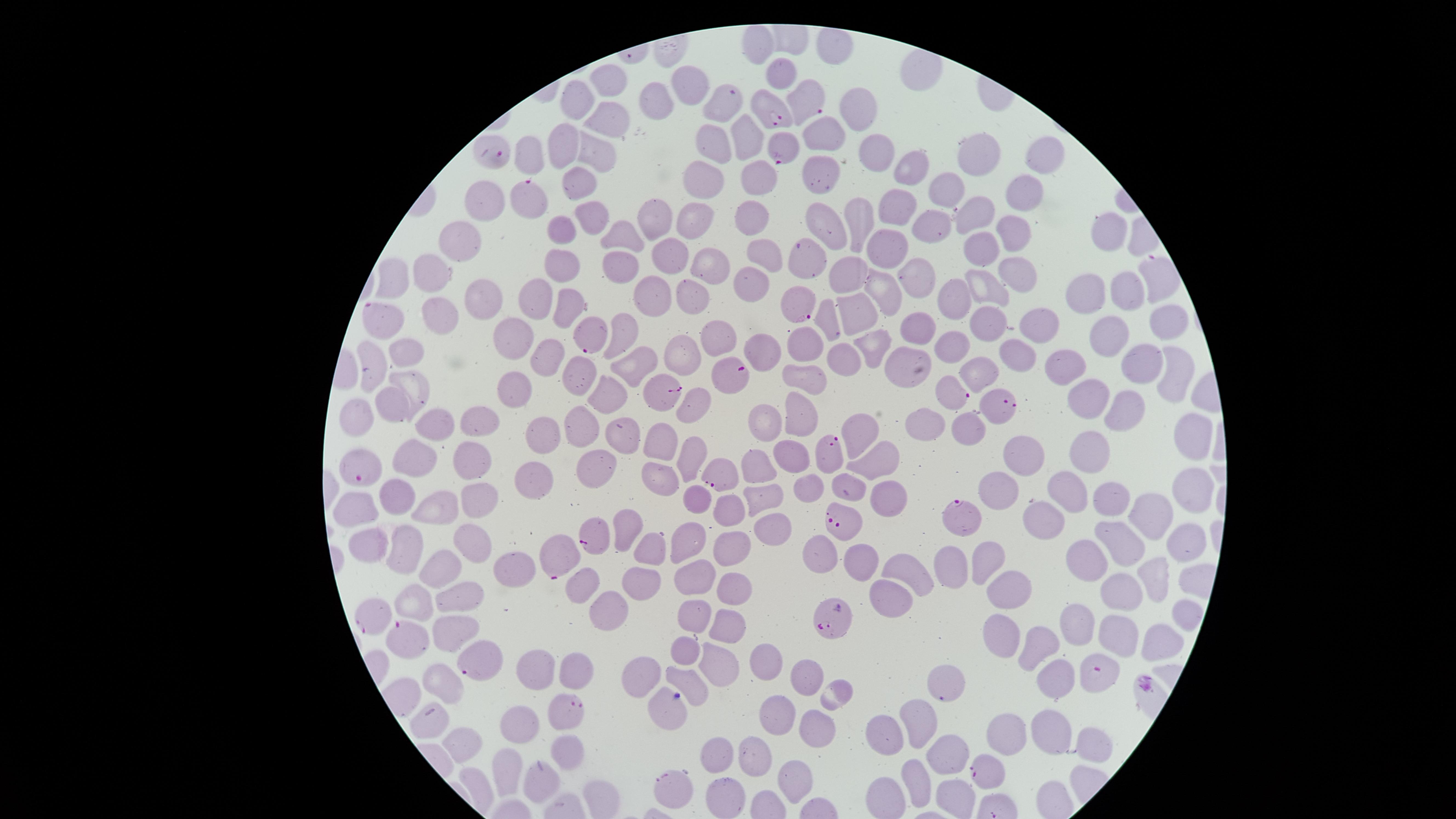
Approximate marker points as {x, y} in pixels. Parasitized red blood cells: {808, 101}, {723, 104}, {772, 110}, {497, 152}, {785, 152}, {525, 196}, {802, 314}, {383, 321}, {590, 337}, {732, 373}, {660, 393}, {952, 394}, {997, 407}, {825, 447}, {359, 467}, {719, 473}, {958, 512}, {846, 525}, {593, 533}, {556, 553}, {829, 615}, {378, 616}, {410, 641}, {479, 659}, {1100, 672}, {573, 711}, {990, 776}, {673, 787}. Uninfected red blood cells: {757, 41}, {781, 70}, {606, 84}, {688, 87}, {578, 100}, {653, 103}, {857, 113}, {613, 116}, {823, 133}, {749, 139}, {715, 140}, {566, 146}, {880, 150}, {597, 152}, {978, 155}, {1047, 155}, {529, 159}, {917, 170}, {760, 174}, {824, 174}, {579, 176}, {705, 179}, {1023, 187}, {949, 188}, {484, 205}, {896, 208}, {976, 209}, {592, 213}, {651, 216}, {754, 216}, {696, 217}, {860, 218}, {926, 225}, {827, 226}, {564, 228}, {1103, 229}, {1011, 230}, {626, 234}, {464, 241}, {888, 248}, {983, 250}, {671, 253}, {805, 256}, {767, 257}, {563, 260}, {620, 263}, {706, 264}, {1015, 265}, {853, 269}, {922, 276}, {397, 278}, {426, 279}, {749, 279}, {1123, 284}, {983, 288}, {1085, 289}, {649, 290}, {879, 292}, {688, 294}, {956, 295}, {480, 296}, {537, 299}, {564, 305}, {438, 309}, {860, 309}, {828, 318}, {989, 319}, {1163, 320}, {915, 325}, {1035, 330}, {1110, 331}, {515, 333}, {625, 334}, {711, 335}, {800, 343}, {870, 345}, {951, 346}, {763, 352}, {677, 353}, {410, 355}, {548, 355}, {1022, 356}, {845, 357}, {635, 359}, {900, 361}, {373, 362}, {1143, 364}, {1171, 365}, {1062, 368}, {986, 374}, {806, 378}, {578, 379}, {415, 385}, {514, 391}, {608, 398}, {1093, 399}, {397, 400}, {1126, 405}, {697, 407}, {800, 411}, {359, 413}, {763, 423}, {969, 423}, {436, 426}, {476, 426}, {923, 426}, {545, 431}, {580, 431}, {1195, 432}, {861, 434}, {623, 436}, {664, 441}, {1086, 451}, {1023, 452}, {696, 453}, {790, 456}, {880, 456}, {422, 463}, {757, 465}, {476, 467}, {658, 473}, {596, 476}, {534, 480}, {806, 484}, {1071, 487}, {1192, 489}, {852, 490}, {996, 491}, {397, 495}, {765, 495}, {483, 498}, {1111, 498}, {436, 503}, {698, 503}, {889, 505}, {730, 509}, {359, 512}, {1043, 513}, {1150, 514}, {627, 525}, {773, 526}, {692, 537}, {1123, 539}, {372, 546}, {1183, 546}, {647, 547}, {406, 549}, {734, 550}, {1092, 553}, {477, 554}, {821, 554}, {982, 560}, {861, 563}, {953, 567}, {520, 570}, {912, 575}, {694, 576}, {1150, 577}, {642, 579}, {443, 581}, {1012, 588}, {585, 589}, {731, 589}, {1120, 593}, {892, 594}, {460, 600}, {417, 604}, {1185, 611}, {609, 616}, {695, 617}, {1085, 619}, {724, 624}, {1118, 627}, {448, 630}, {1039, 637}, {1000, 639}, {1159, 641}, {683, 652}, {764, 658}, {715, 662}, {535, 670}, {578, 673}, {642, 674}, {806, 676}, {945, 677}, {444, 679}, {689, 679}, {1056, 680}, {836, 687}, {664, 709}, {779, 713}, {916, 717}, {1050, 725}, {518, 726}, {427, 727}, {810, 727}, {1014, 731}, {892, 736}, {466, 742}, {1096, 744}, {567, 747}, {950, 752}, {716, 758}, {750, 758}, {503, 767}, {794, 777}, {917, 781}, {539, 786}, {952, 798}, {725, 806}. One field of view of the specimen. Presence: malaria parasites detected. Image is 1456×819 pixels. Giemsa stain. The visible region is circular. Thin blood film. Photographed with a smartphone camera through the microscope eyepiece. Species: Plasmodium falciparum.